Describe the morphology of the erythrocytes.
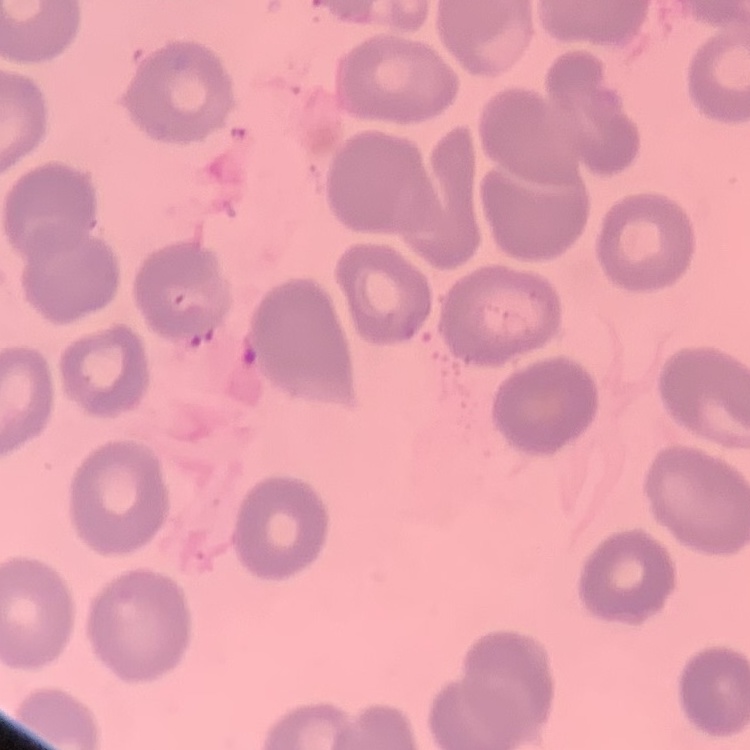

They show no rouleaux formation.

Field's or Giemsa stain. Thin blood film. Square crop of a larger photomicrograph.